Name the parasite shown.
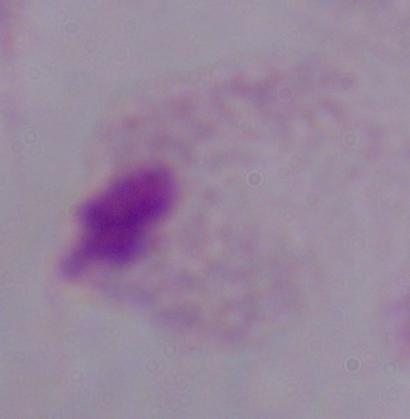
A trichomonad.

magnification = 1000x
modality = micrograph